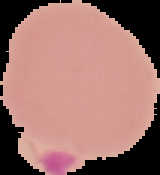

Summary:
  - Malaria status: uninfected
  - Image type: segmented cell region with the area outside set to black
  - Preparation: thin blood film
  - Image size: 160×175 pixels